Report the malaria status of this cell.
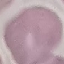
It is uninfected.

{
  "stain": "Giemsa",
  "image_type": "automatically extracted cell patch, resized to 64 × 64 pixels",
  "capture": "smartphone camera at the microscope eyepiece",
  "preparation": "thin blood film"
}